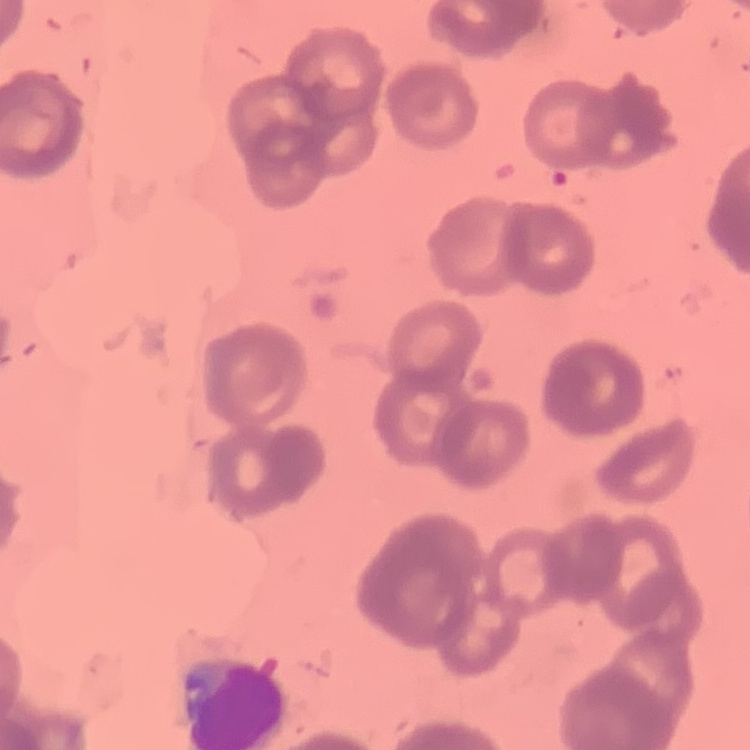
The erythrocytes exhibit rouleaux formation. Thin blood film. Field's or Giemsa stain. Square crop of a larger photomicrograph.